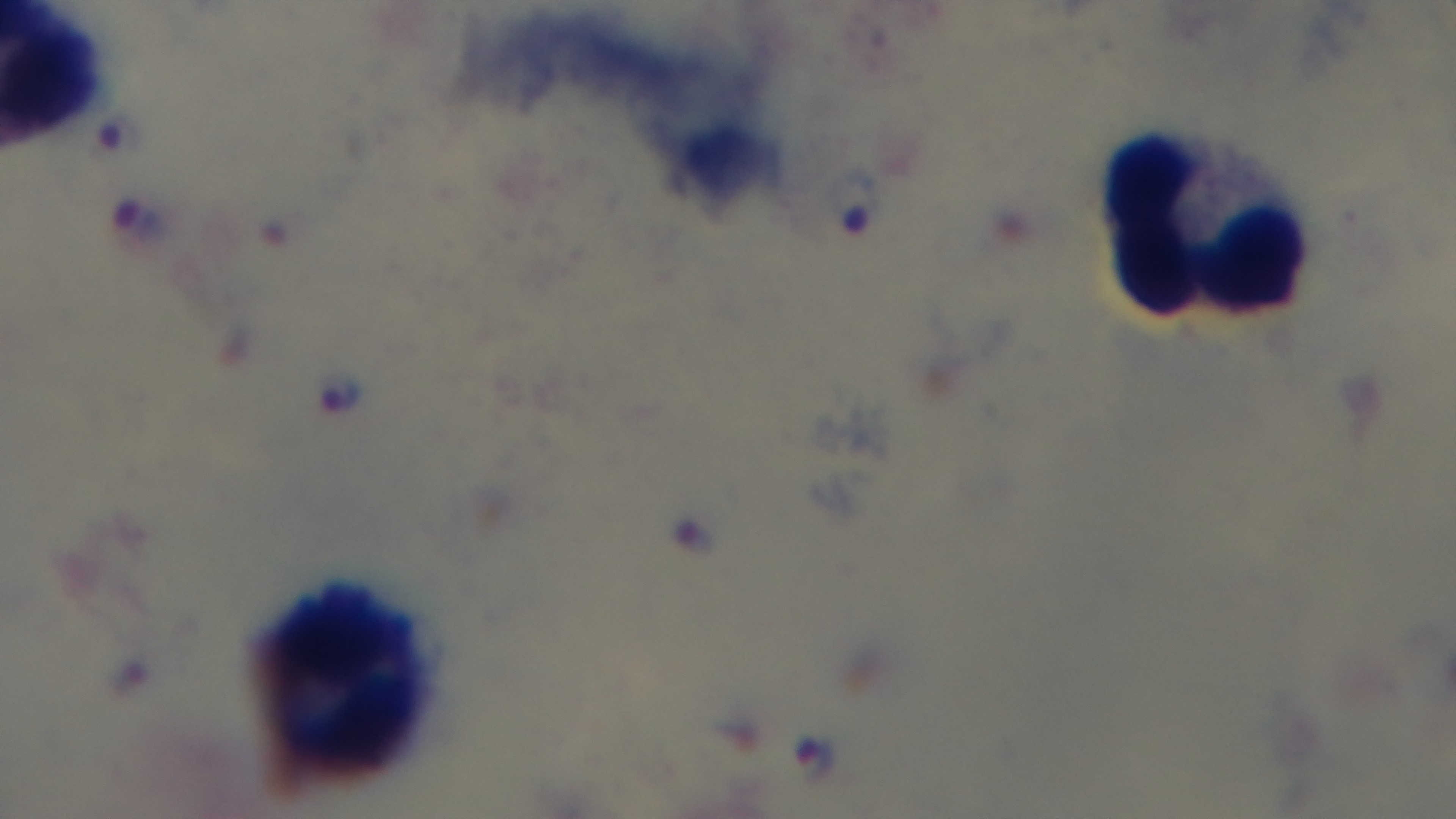
malaria_status: infected
preparation: thick smear
stain: Giemsa
objective: 100x oil immersion
field_of_view: one from the slide
capture: mounted 4K digital camera
modality: light microscopy